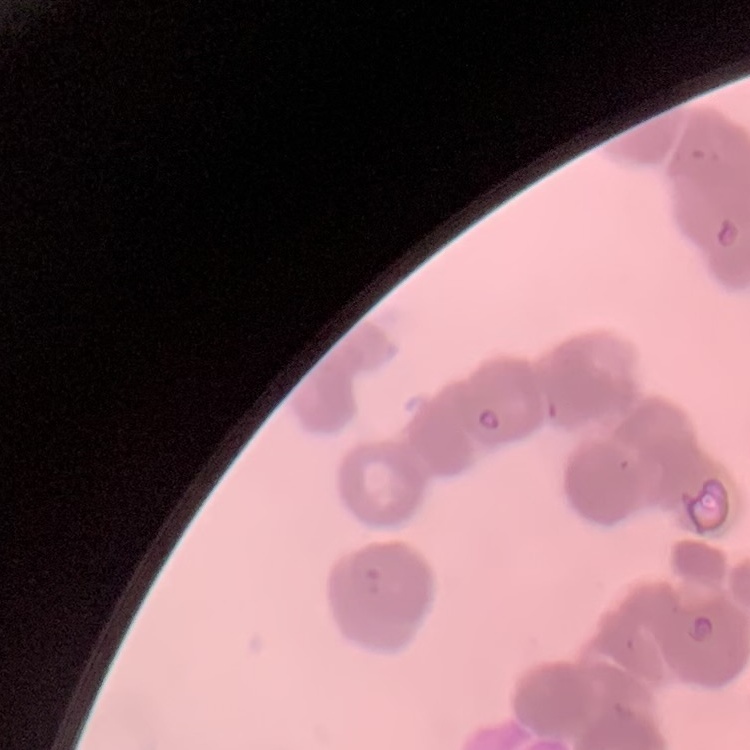
The erythrocytes exhibit rouleaux formation. One tile cut from a larger photomicrograph. Field's or Giemsa stain. Thin blood smear.